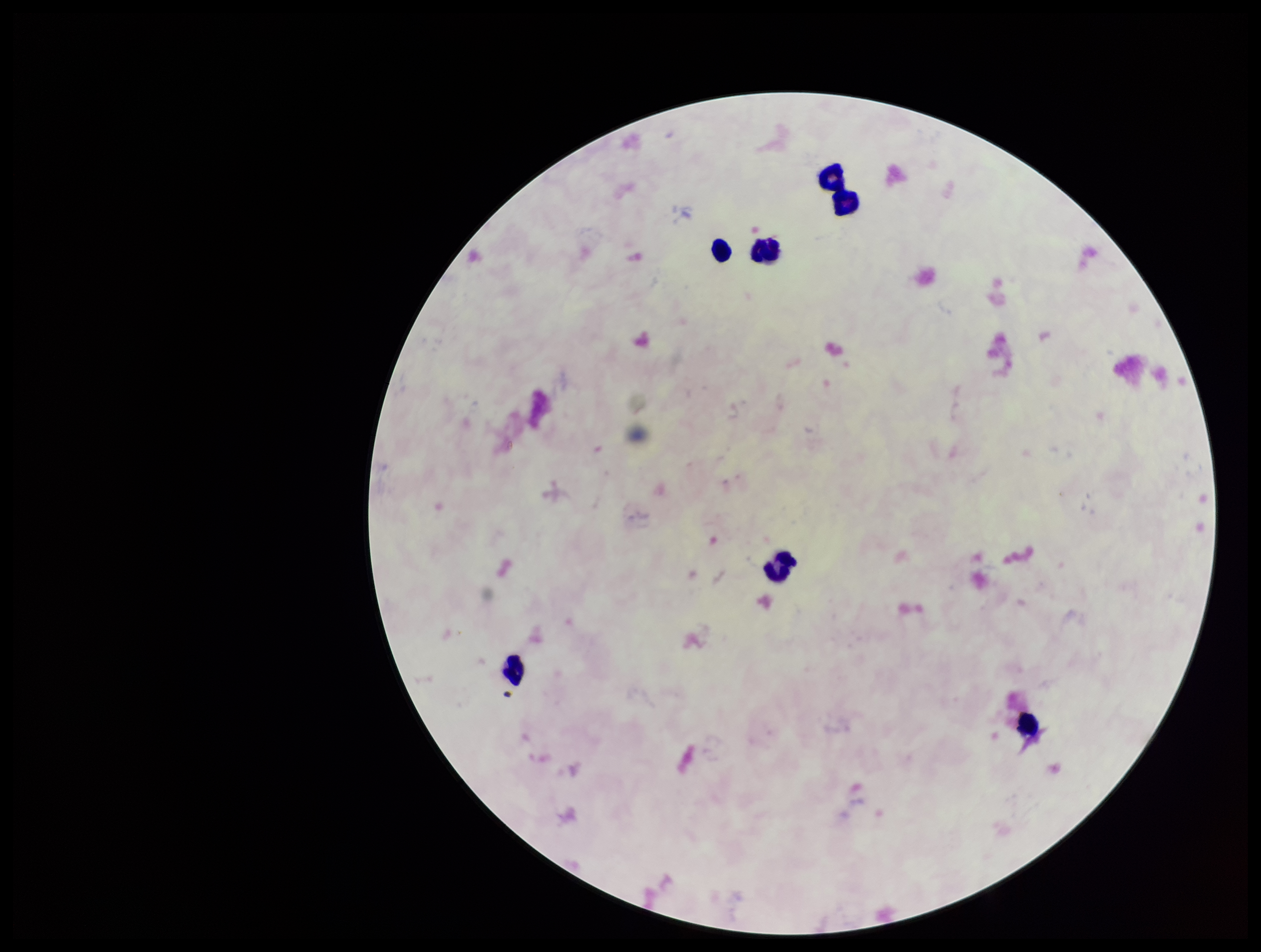

Plasmodium parasites: none identified. One field from this slide. Image is 1261×952 pixels. Leukocyte count: 7. Patient malaria status: negative. Parasite count: 0. Giemsa stain. Preparation: thick smear. Photographed through the microscope eyepiece with a smartphone camera.